Locate every blood parasite and identify its species.
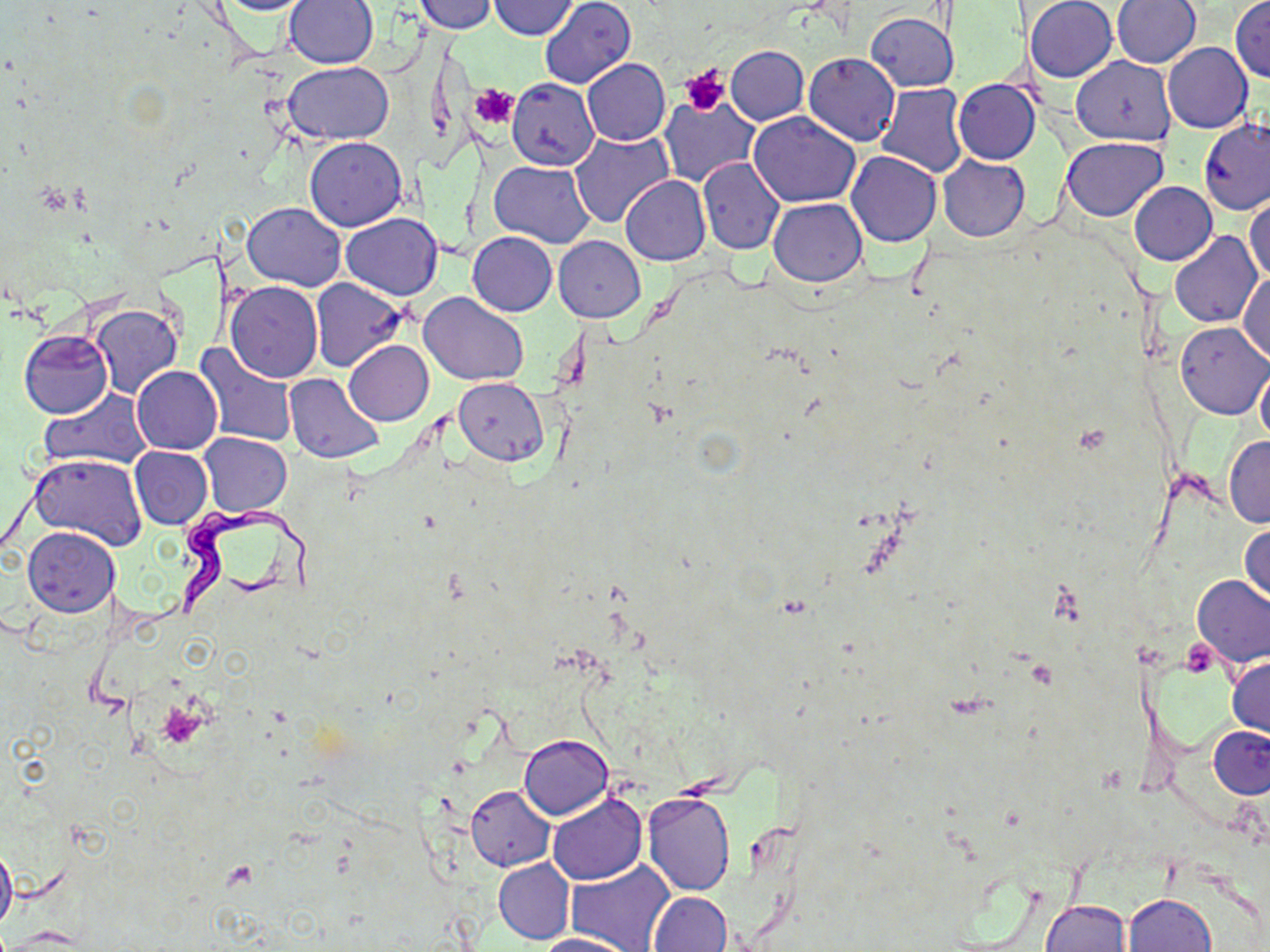

Approximate bounding boxes as (x1,y1)-(x2,y2) corner pairs in pixels.
Trypanosoma brucei: (176,506)-(325,622).
No Plasmodium falciparum, Plasmodium ovale, Plasmodium malariae, Plasmodium vivax, or Babesia divergens observed.

Summary:
  - Uninfected red blood cell locations: (207,0)-(316,15), (540,0)-(635,89), (1025,0)-(1118,83), (1112,0)-(1201,67), (1230,0)-(1270,82), (283,1)-(377,70), (418,1)-(494,32), (490,1)-(579,39), (865,13)-(959,91), (1162,43)-(1252,133), (725,46)-(808,125), (804,53)-(900,146), (1072,56)-(1176,145), (581,58)-(670,146), (282,60)-(393,144), (952,78)-(1039,165), (507,79)-(599,169), (876,83)-(967,178), (659,95)-(758,186), (748,111)-(859,207), (1198,117)-(1269,216), (570,130)-(675,229), (305,136)-(408,231), (1062,138)-(1167,221), (846,150)-(941,248), (938,155)-(1029,241), (698,156)-(784,255), (490,160)-(596,247), (620,175)-(711,266), (1130,181)-(1217,265), (1246,193)-(1270,287), (770,198)-(866,287), (243,202)-(346,290), (340,214)-(442,300), (467,231)-(556,316), (1171,232)-(1262,327), (553,236)-(645,323), (1238,271)-(1269,364), (311,278)-(408,372), (225,281)-(322,383), (418,292)-(527,385), (88,304)-(183,400), (1176,321)-(1270,419), (19,330)-(113,418), (344,340)-(433,425), (193,343)-(299,448), (131,365)-(223,454), (1256,367)-(1270,447), (285,374)-(384,463), (453,378)-(549,465), (39,389)-(152,471), (199,432)-(292,516), (1223,435)-(1270,528), (128,447)-(213,529), (29,454)-(147,550), (1240,522)-(1269,608), (23,527)-(120,617), (1193,576)-(1270,667), (1227,656)-(1269,739), (1209,725)-(1270,798), (519,734)-(613,819), (466,785)-(555,871), (643,791)-(736,895), (547,792)-(647,884), (0,842)-(17,935), (494,859)-(574,944), (566,862)-(675,952), (647,891)-(732,952), (1121,893)-(1216,952), (1041,898)-(1131,952), (535,933)-(636,952)
  - Platelet locations: (680,64)-(729,115), (470,84)-(518,129)
  - Slide-level diagnosis: Trypanosoma brucei
  - Preparation: thin blood film
  - Stain: May-Grünwald-Giemsa
  - Field of view: one of a larger specimen
  - Magnification: 1000x
  - Modality: optical microscopy
  - Image size: 1270×952 pixels